Name the blood parasite species.
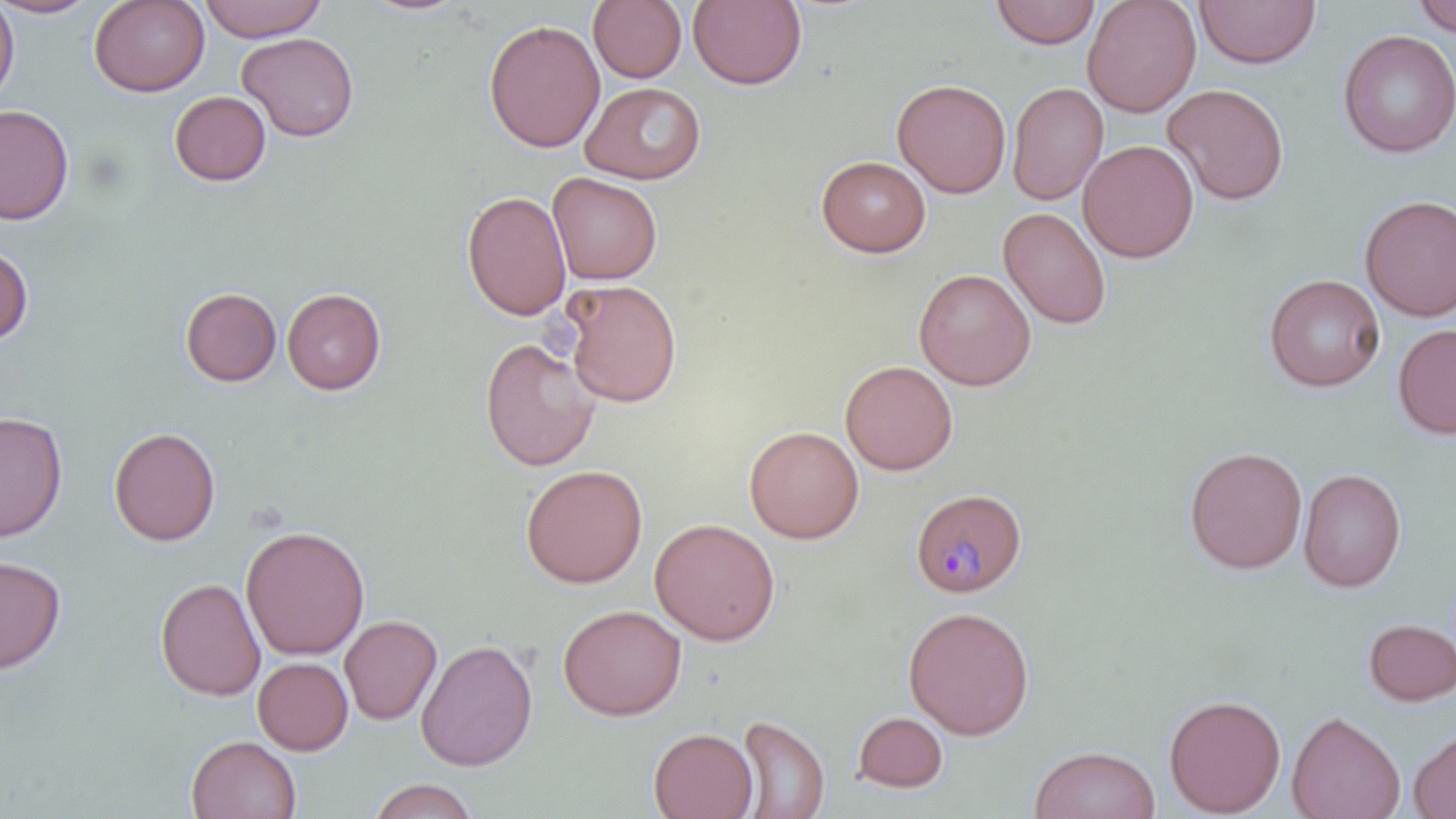
Plasmodium malariae.

field_of_view: one of a larger specimen
magnification: 1000x
uninfected_red_blood_cell_locations: 'approximate bounding boxes as (x1, y1, x2, y2) in pixels: (0, 0, 19, 103), (0, 0, 101, 18), (89, 0, 210, 97), (198, 0, 326, 41), (588, 0, 687, 83), (688, 0, 808, 91), (990, 0, 1100, 48), (1082, 0, 1200, 117), (1194, 0, 1321, 68), (1410, 0, 1456, 37), (362, 1, 468, 16), (483, 18, 604, 153), (1337, 30, 1456, 158), (237, 32, 359, 142), (892, 78, 1011, 198), (581, 81, 706, 183), (1007, 82, 1108, 206), (1162, 83, 1290, 205), (169, 91, 272, 186), (0, 104, 74, 225), (1078, 140, 1198, 263), (816, 155, 931, 257), (548, 172, 662, 285), (461, 190, 571, 322), (1359, 194, 1456, 321), (998, 207, 1111, 329), (0, 244, 33, 346), (914, 269, 1036, 390), (1264, 274, 1385, 392), (562, 280, 682, 408), (180, 287, 282, 386), (282, 288, 386, 395), (1393, 323, 1456, 440), (480, 337, 600, 471), (840, 360, 958, 475), (0, 411, 67, 542), (744, 425, 864, 544), (108, 426, 221, 546), (1184, 445, 1307, 574), (520, 464, 648, 588), (1298, 467, 1406, 593), (649, 517, 780, 646), (240, 524, 370, 660), (0, 555, 65, 673), (155, 577, 265, 701), (558, 604, 686, 721), (902, 605, 1034, 739), (340, 615, 442, 725), (1362, 618, 1456, 706), (415, 638, 538, 771), (252, 657, 353, 755), (1163, 693, 1286, 817), (1287, 710, 1406, 819), (853, 712, 948, 793), (735, 714, 830, 818), (648, 727, 758, 819), (1409, 729, 1456, 818), (187, 735, 301, 819), (1029, 745, 1160, 819), (368, 778, 478, 819)'
preparation: thin blood smear
plasmodium_malariae_infected_red_blood_cell_locations: 'approximate bounding boxes as (x1, y1, x2, y2) in pixels: (911, 488, 1027, 598)'
modality: optical microscopy
image_size: 1456×819 pixels
stain: May-Grünwald-Giemsa